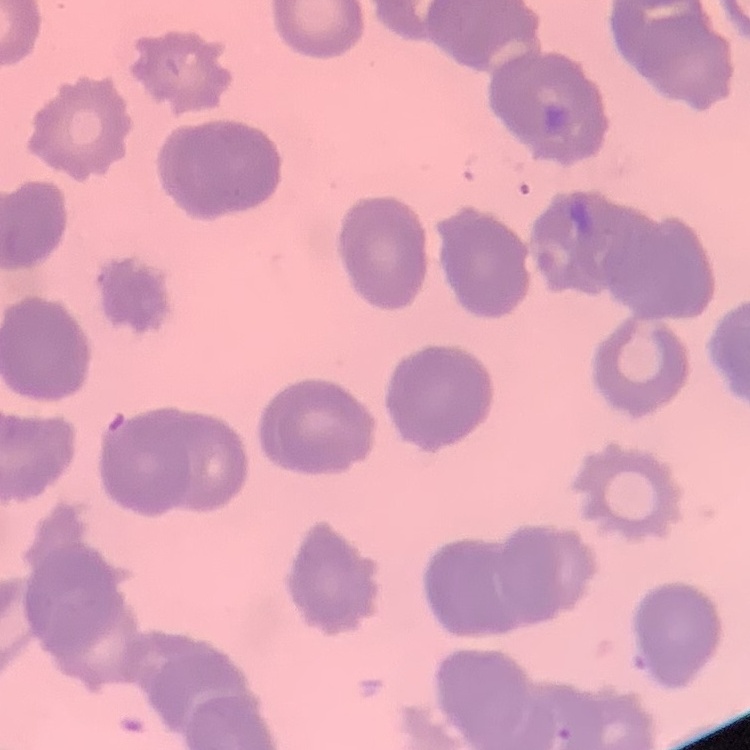
{
  "erythrocyte_morphology": "rouleaux formation",
  "stain": "Field's or Giemsa",
  "preparation": "thin peripheral smear",
  "image_type": "square crop of a larger photomicrograph"
}